Report the malaria status of this cell.
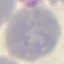
It is uninfected.

image type = cell patch, automatically extracted from a larger field of view and resized to 64 × 64 pixels
preparation = thin smear
stain = Giemsa
capture = smartphone through the microscope eyepiece